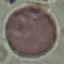
{
  "result": "no malaria parasites detected",
  "capture": "smartphone camera at the microscope eyepiece",
  "stain": "Giemsa",
  "image_type": "cell patch, automatically extracted from a larger field of view and resized to 64 × 64 pixels",
  "preparation": "thin smear"
}